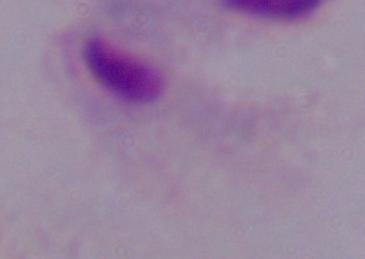

Photomicrograph. Captured at 1000x magnification. A trichomonad is seen.